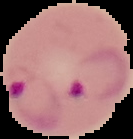
Segmented cell region on a black background. Image is 133×139 pixels. From a thin blood film. Result: Plasmodium parasites identified.